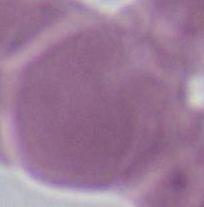 Micrograph. Captured at 1000x magnification. A red blood cell is shown.